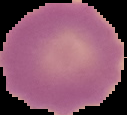
Image is 127×115 pixels. Result: negative for malaria parasites. Cell region segmented out of the field of view; the surrounding area is masked to black. From a thin blood smear.